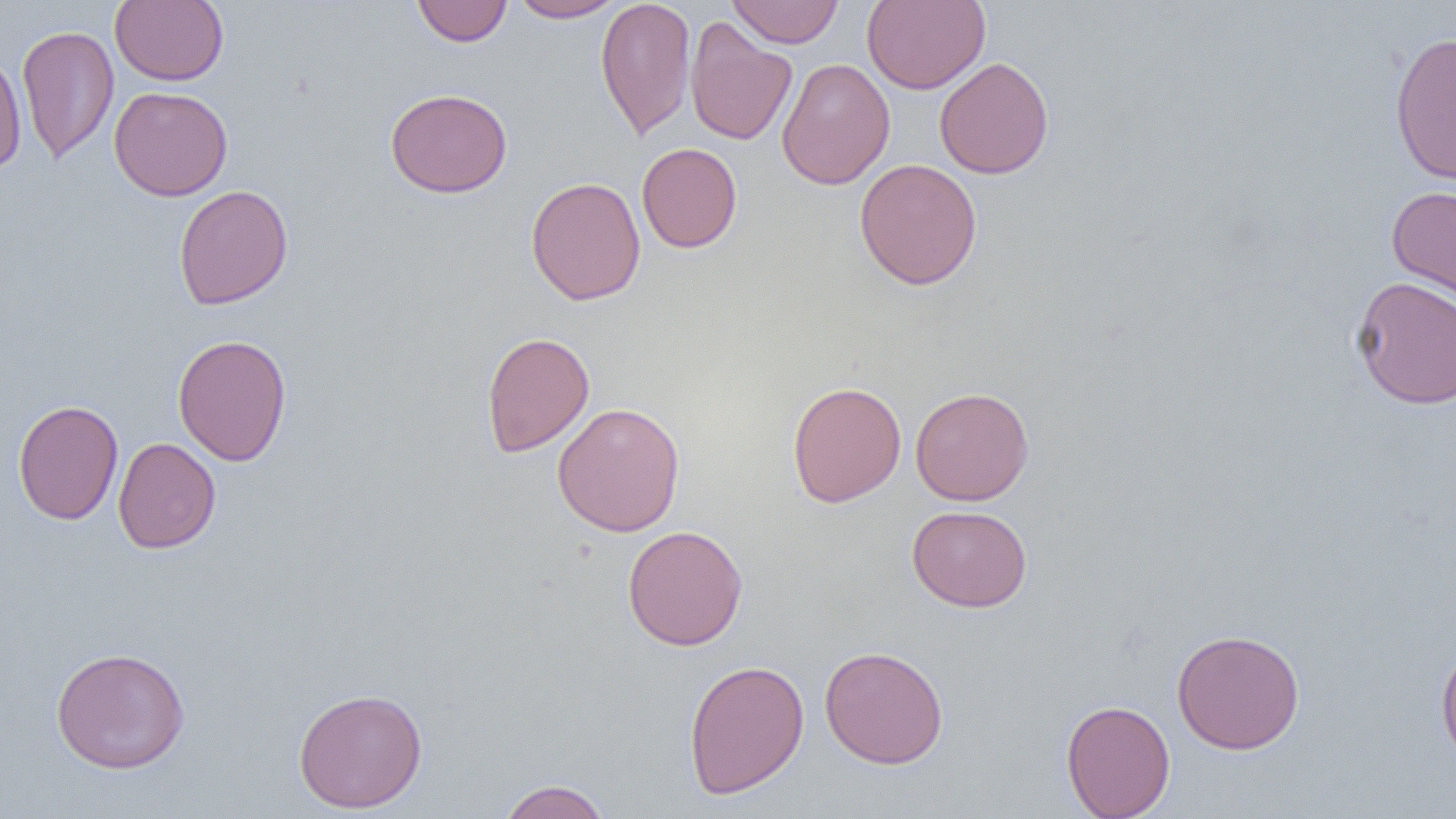

slide_level_diagnosis: negative for blood parasites
modality: optical microscopy
magnification: 1000x
image_size: 1456×819 pixels
field_of_view: single
uninfected_red_blood_cell_locations: 'approximate bounding boxes as (x1, y1, x2, y2) in pixels: (110, 0, 229, 86), (412, 0, 513, 46), (509, 0, 628, 22), (595, 0, 696, 141), (727, 0, 844, 48), (862, 1, 990, 94), (685, 17, 797, 147), (16, 24, 119, 165), (1389, 31, 1456, 186), (0, 50, 27, 175), (934, 57, 1054, 179), (777, 58, 895, 190), (108, 86, 233, 201), (384, 88, 513, 198), (636, 143, 743, 253), (854, 158, 982, 290), (525, 176, 646, 306), (173, 184, 294, 310), (1386, 185, 1456, 312), (1350, 275, 1456, 410), (481, 331, 595, 458), (173, 333, 291, 467), (786, 380, 907, 508), (909, 386, 1034, 506), (12, 400, 123, 525), (552, 402, 685, 537), (112, 437, 221, 554), (906, 505, 1032, 612), (622, 525, 748, 650), (1171, 628, 1305, 755), (1435, 640, 1456, 769), (819, 644, 949, 769), (50, 646, 190, 774), (683, 659, 810, 799), (293, 686, 428, 814), (1061, 699, 1175, 819), (497, 779, 611, 819)'
preparation: thin blood film